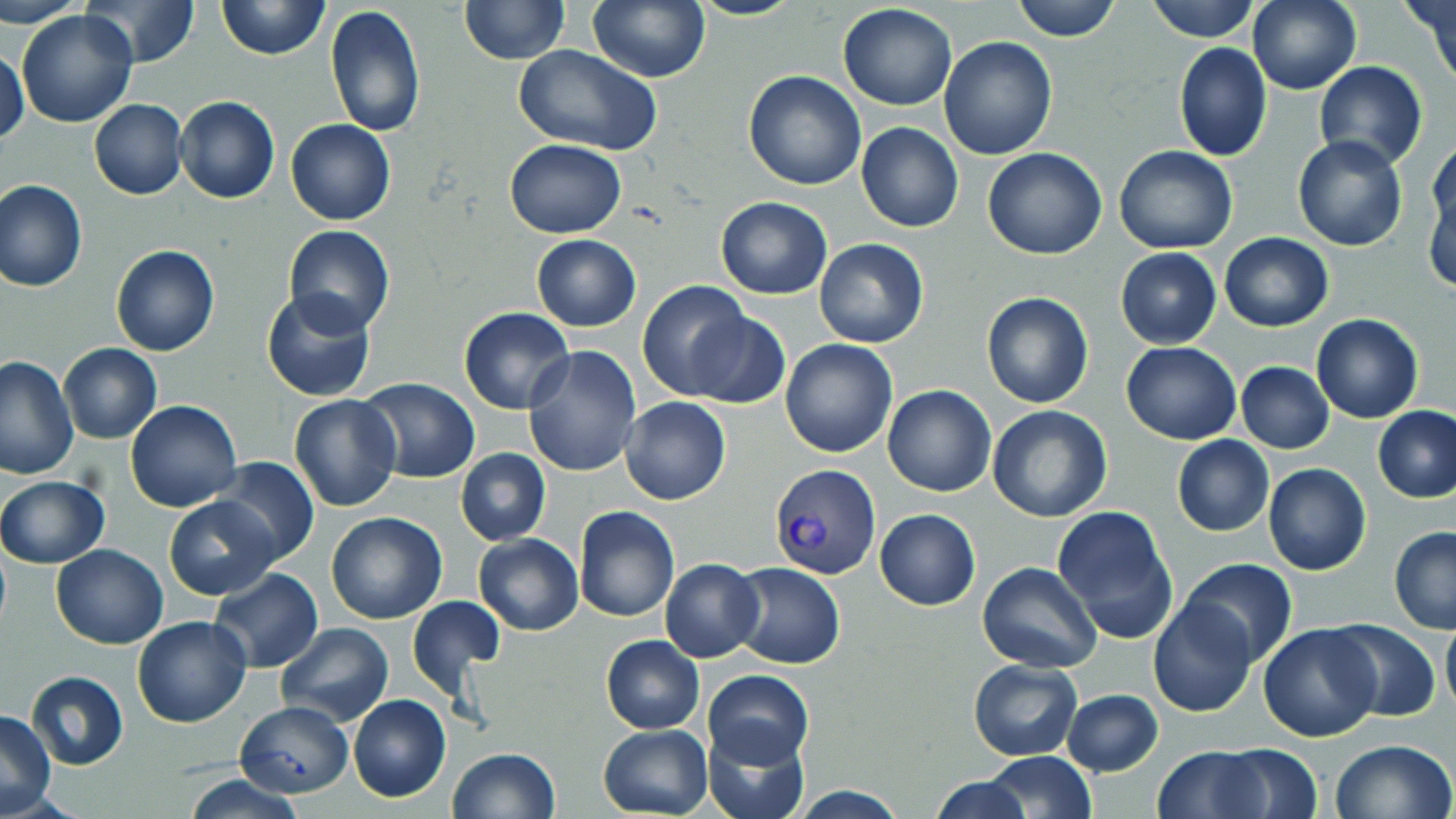 Approximate bounding boxes as [x1, y1, x2, y2] in pixels. Uninfected red blood cell locations: [4, 0, 87, 28], [81, 0, 201, 68], [217, 0, 329, 59], [587, 0, 709, 82], [1011, 0, 1122, 42], [1148, 0, 1260, 42], [1248, 0, 1362, 95], [1406, 0, 1455, 83], [458, 1, 571, 64], [836, 2, 959, 110], [325, 5, 427, 138], [16, 10, 137, 129], [939, 36, 1058, 160], [1173, 41, 1272, 163], [514, 44, 663, 159], [1, 45, 29, 148], [1313, 61, 1428, 170], [743, 70, 867, 190], [175, 97, 280, 204], [89, 99, 187, 200], [285, 119, 395, 226], [857, 122, 963, 233], [1292, 134, 1409, 250], [1429, 136, 1456, 237], [504, 138, 626, 239], [1113, 145, 1237, 254], [982, 148, 1108, 260], [1424, 178, 1456, 295], [1, 179, 88, 290], [716, 197, 833, 299], [283, 225, 394, 336], [1219, 232, 1334, 330], [531, 234, 641, 331], [813, 239, 928, 349], [110, 245, 219, 356], [1115, 248, 1222, 348], [638, 280, 754, 400], [261, 288, 378, 402], [980, 292, 1095, 409], [460, 307, 573, 414], [684, 312, 789, 410], [1311, 313, 1424, 424], [780, 338, 897, 458], [1121, 341, 1242, 445], [58, 343, 161, 443], [523, 347, 642, 477], [1, 356, 79, 480], [1235, 361, 1335, 453], [358, 378, 479, 485], [883, 385, 996, 497], [288, 394, 402, 511], [620, 397, 731, 504], [126, 400, 242, 513], [986, 404, 1113, 523], [1372, 405, 1455, 504], [1172, 435, 1274, 536], [456, 449, 550, 546], [212, 457, 318, 567], [1262, 463, 1371, 577], [0, 474, 109, 567], [165, 496, 276, 599], [572, 505, 680, 623], [875, 508, 980, 610], [1053, 508, 1174, 641], [326, 511, 448, 624], [1389, 527, 1456, 633], [473, 533, 583, 636], [50, 543, 169, 648], [1179, 557, 1298, 667], [659, 558, 763, 663], [729, 562, 846, 669], [979, 562, 1101, 672], [211, 568, 324, 672], [407, 596, 504, 698], [1148, 598, 1258, 717], [1441, 614, 1456, 719], [131, 615, 251, 729], [1328, 619, 1442, 722], [276, 622, 394, 726], [1258, 624, 1382, 742], [602, 635, 704, 733], [968, 658, 1082, 761], [703, 670, 814, 770], [25, 671, 129, 769], [1063, 689, 1163, 775], [348, 695, 452, 802], [234, 700, 354, 799], [1, 708, 57, 815], [598, 724, 711, 818], [701, 727, 809, 819], [1330, 739, 1456, 819], [1211, 742, 1324, 817], [1154, 744, 1270, 818], [447, 748, 560, 819], [982, 751, 1096, 817], [179, 774, 306, 819], [930, 776, 1033, 818], [784, 787, 909, 817]. Plasmodium vivax-infected red blood cell locations: [770, 463, 881, 579]. Slide-level diagnosis: Plasmodium vivax. Thin blood smear. Optical microscopy. One field of a larger specimen. Image is 1456×819 pixels. May-Grünwald-Giemsa-stained preparation. 1000x magnification.